Name the parasite shown.
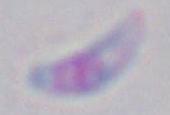
This is Toxoplasma gondii.

Captured at 1000x magnification. Photomicrograph.